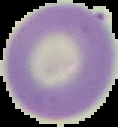
From a thin blood smear. Image is 118×127 pixels. Segmented cell region on a black background. Result: negative for Plasmodium parasites.